Assess this cell for malaria.
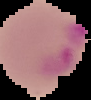

Parasitized.

Image is 91×100 pixels. Segmented cell region on a black background. From a thin blood film.